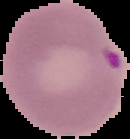

image_type: segmented cell region with the area outside set to black
image_size: 130×139 pixels
malaria_status: parasitized
preparation: thin blood film